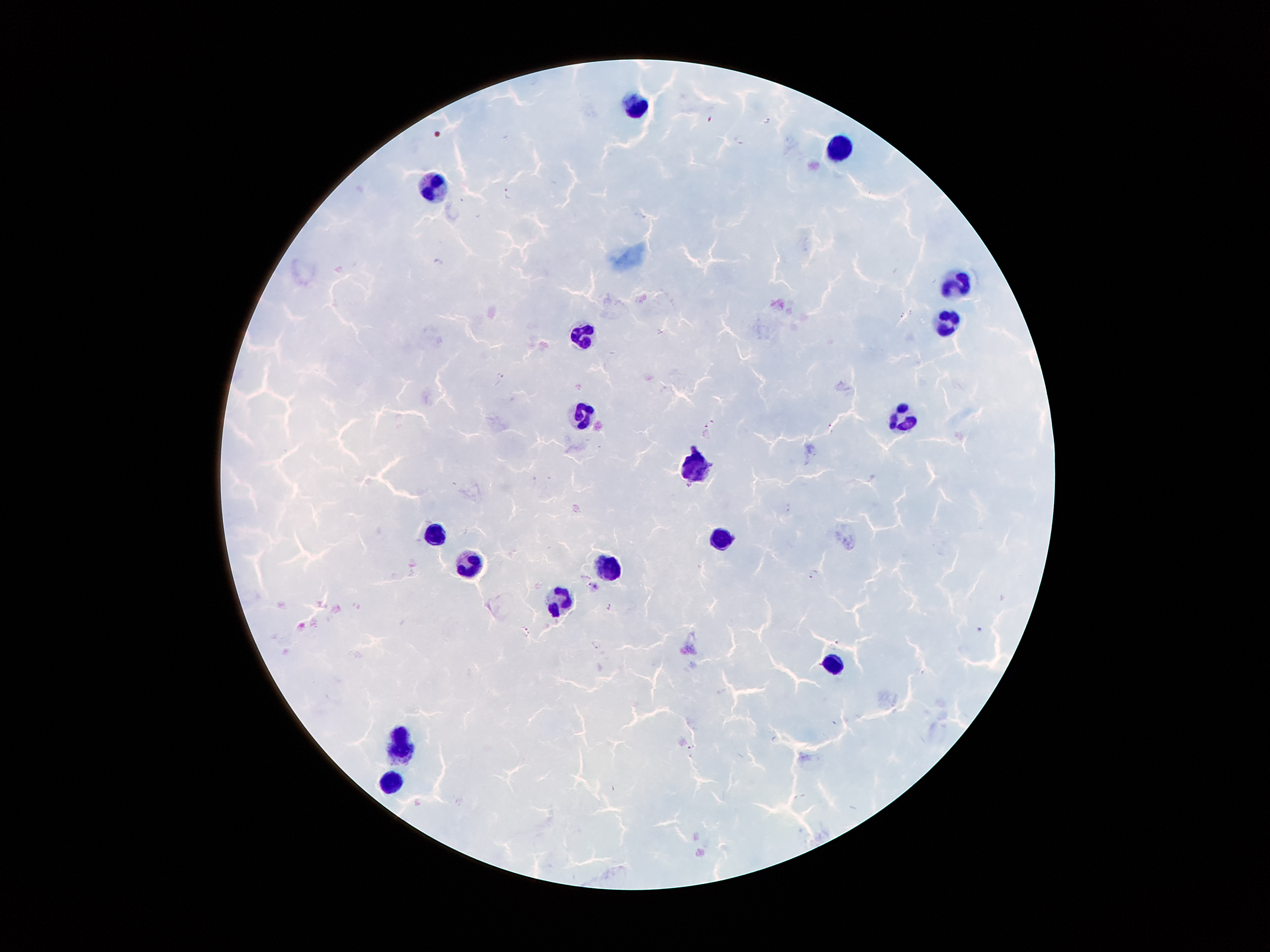
Approximate object centers, in pixels from the top-left corner. Leukocyte locations: (x=635, y=107), (x=837, y=148), (x=433, y=186), (x=956, y=287), (x=945, y=320), (x=585, y=339), (x=585, y=417), (x=907, y=419), (x=700, y=467), (x=434, y=535), (x=723, y=538), (x=468, y=562), (x=606, y=570), (x=559, y=599), (x=834, y=667), (x=405, y=746), (x=392, y=782). Malaria parasite locations: (x=767, y=120), (x=740, y=140), (x=510, y=193), (x=440, y=261), (x=500, y=377), (x=712, y=420), (x=705, y=425), (x=814, y=575), (x=610, y=607), (x=979, y=629), (x=525, y=631), (x=596, y=644), (x=834, y=645), (x=692, y=746). 100x magnification. Thick peripheral-blood smear. Image is 1270×952 pixels. Patient malaria status: infected with Plasmodium falciparum. Single field of view. Smartphone photograph taken through the microscope eyepiece. Giemsa-stained preparation.